Give the position of every leukocyte visible.
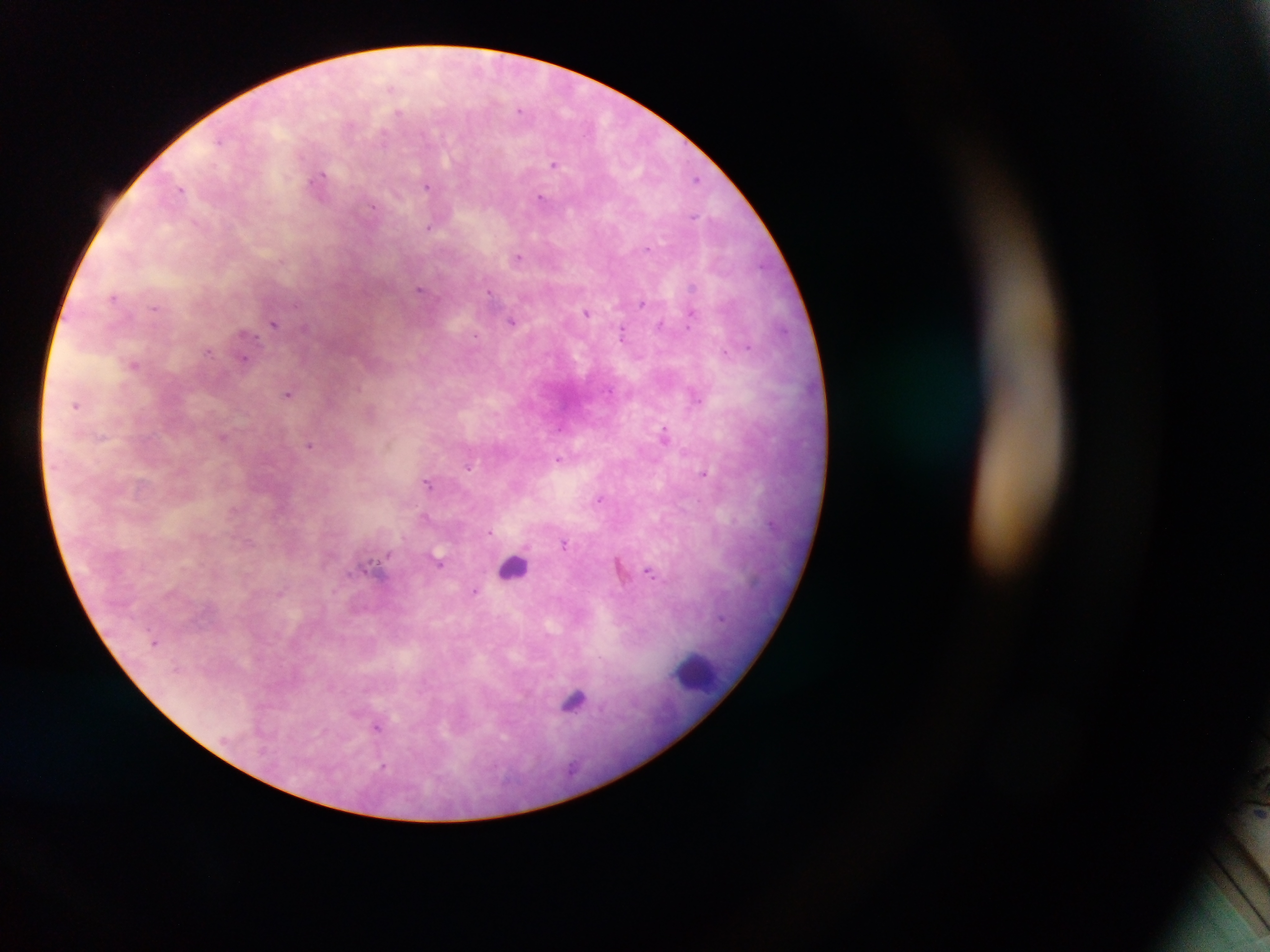
Approximate centers as x y in pixels.
Leukocytes: 511 568; 693 674.

field of view = single
country = Ghana
capture = mobile-phone photograph through a microscope
Plasmodium parasite locations = approximate centers as x y in pixels: 520 110; 555 162; 319 176; 696 178; 426 187; 182 188; 541 197; 431 227; 518 258; 420 288; 693 288; 114 296; 642 304; 156 308; 587 313; 691 319; 512 320; 276 323; 662 325; 622 335; 724 349; 209 352; 245 356; 134 365; 290 391; 695 397; 77 405; 561 427; 664 433; 223 435; 389 442; 310 445; 559 458; 471 467; 705 473; 429 483; 599 499; 424 516; 489 532; 567 544; 387 555; 440 561; 619 566; 653 572; 475 590; 721 619; 527 691; 576 702; 377 726
image size = 1270×952 pixels
preparation = thick blood smear